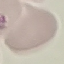

Summary:
  - Malaria status: uninfected
  - Preparation: thin smear
  - Capture: smartphone through the microscope eyepiece
  - Stain: Giemsa
  - Image type: automatically extracted cell patch, resized to 64 × 64 pixels